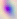
modality = photomicrograph
identification = Toxoplasma gondii
magnification = 400x